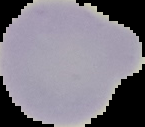

Summary:
  - Preparation: thin blood smear
  - Image size: 145×127 pixels
  - Result: negative for Plasmodium parasites
  - Image type: segmented cell region with the area outside set to black